Locate and identify every blood parasite.
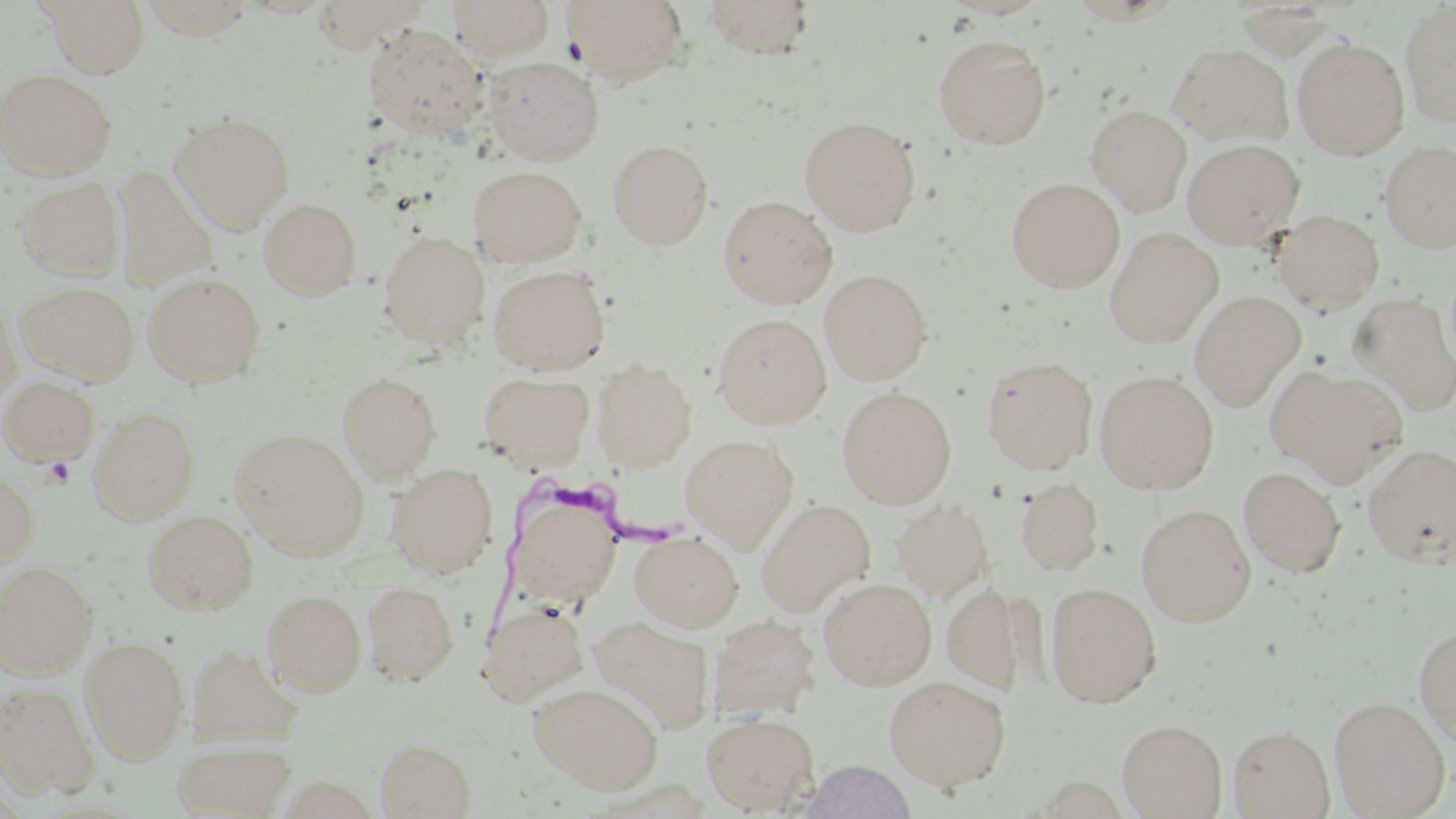

Approximate bounding boxes as (x1, y1, x2, y2) in pixels.
Trypanosoma brucei: (480, 460, 692, 656).
No Plasmodium falciparum, Plasmodium ovale, Plasmodium malariae, Plasmodium vivax, or Babesia divergens observed.

Summary:
  - Uninfected red blood cell locations: (43, 0, 150, 77), (447, 0, 555, 60), (562, 0, 687, 85), (702, 0, 816, 58), (1064, 0, 1182, 25), (1400, 2, 1456, 127), (365, 25, 488, 139), (933, 34, 1051, 149), (1293, 38, 1410, 159), (1167, 43, 1293, 144), (482, 56, 604, 165), (0, 69, 117, 180), (1086, 105, 1192, 215), (170, 110, 295, 232), (799, 116, 921, 235), (607, 138, 714, 250), (1183, 139, 1305, 248), (1379, 142, 1456, 253), (113, 164, 219, 292), (469, 165, 586, 267), (16, 177, 125, 280), (1006, 177, 1126, 291), (718, 195, 837, 308), (259, 197, 362, 301), (1273, 210, 1385, 313), (1104, 227, 1223, 347), (379, 230, 490, 346), (489, 264, 609, 374), (820, 269, 932, 385), (143, 272, 265, 386), (17, 280, 139, 384), (1189, 292, 1306, 410), (0, 294, 21, 409), (1349, 294, 1456, 417), (713, 313, 831, 428), (981, 355, 1098, 474), (592, 359, 697, 471), (1268, 365, 1408, 484), (1095, 370, 1219, 493), (337, 372, 442, 481), (479, 372, 595, 472), (1, 376, 99, 466), (837, 386, 957, 507), (89, 406, 199, 523), (231, 429, 370, 559), (680, 434, 799, 551), (1362, 443, 1456, 567), (388, 463, 499, 577), (0, 466, 39, 571), (1238, 466, 1346, 577), (1015, 478, 1104, 575), (510, 493, 621, 608), (755, 498, 876, 617), (890, 498, 994, 603), (1136, 504, 1256, 625), (142, 510, 258, 614), (630, 531, 743, 631), (0, 561, 97, 678), (819, 576, 937, 690), (363, 580, 459, 686), (940, 580, 1029, 694), (1045, 583, 1162, 708), (262, 589, 366, 696), (479, 599, 590, 705), (708, 615, 820, 720), (590, 616, 715, 735), (1414, 625, 1456, 743), (80, 635, 190, 762), (187, 643, 302, 746), (884, 675, 1011, 790), (0, 681, 99, 798), (530, 682, 664, 795), (1329, 696, 1451, 817), (701, 712, 819, 813), (1117, 718, 1227, 818), (1228, 725, 1334, 818), (376, 737, 476, 818), (172, 739, 297, 817), (799, 760, 918, 819)
  - Slide-level diagnosis: Trypanosoma brucei
  - Image size: 1456×819 pixels
  - Stain: May-Grünwald-Giemsa
  - Magnification: 1000x
  - Preparation: thin blood smear
  - Modality: optical microscopy
  - Field of view: one of a larger specimen